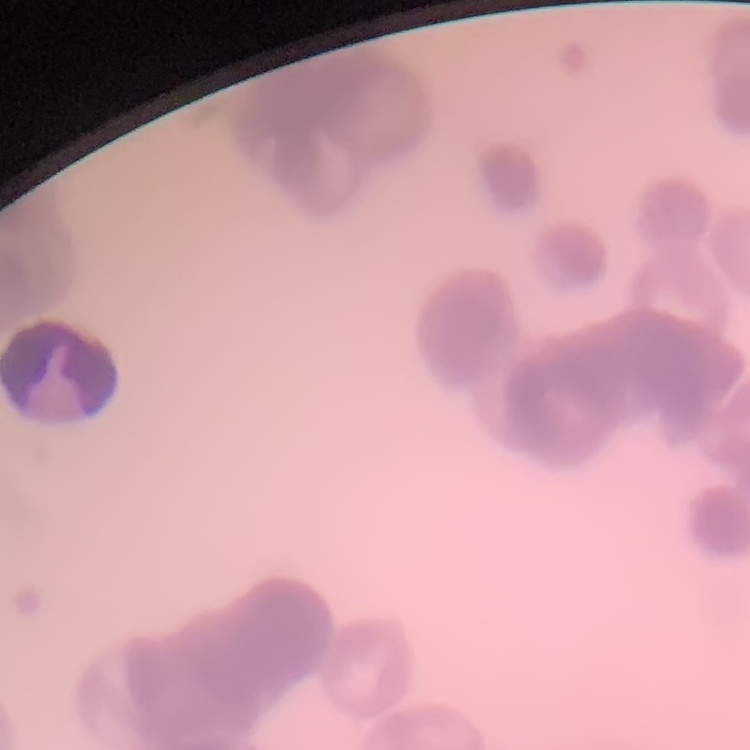
red blood cell morphology = rouleaux formation
stain = Field's or Giemsa
image type = square crop of a larger photomicrograph
preparation = thin peripheral smear